Locate every malaria parasite.
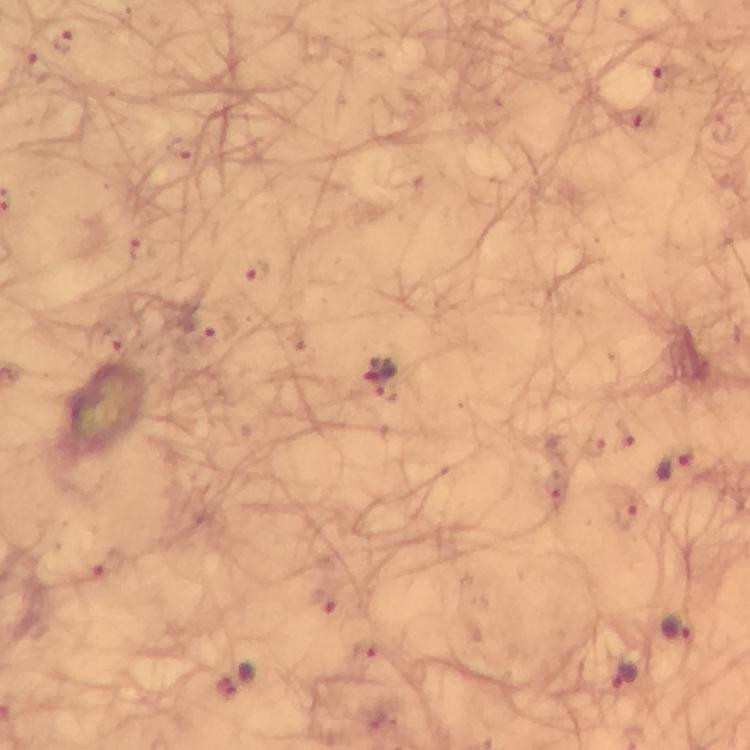

Approximate object centers, in pixels from the top-left corner.
Malaria parasites: (x=63, y=41), (x=38, y=67), (x=667, y=77), (x=184, y=147), (x=257, y=270), (x=207, y=342), (x=114, y=344), (x=383, y=379), (x=676, y=463), (x=555, y=489), (x=625, y=514), (x=325, y=601), (x=677, y=627), (x=367, y=649), (x=624, y=673).

immersion oil = applied
magnification = 100x
context = from a malaria diagnostic workup
stain = Giemsa
image size = 750×750 pixels
capture = smartphone camera through the microscope
cropped from = a single field of view
preparation = thick blood smear